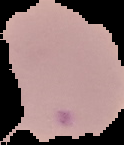

Summary:
  - Result: Plasmodium parasites detected
  - Preparation: thin blood film
  - Image size: 124×145 pixels
  - Image type: segmented cell region with the area outside set to black